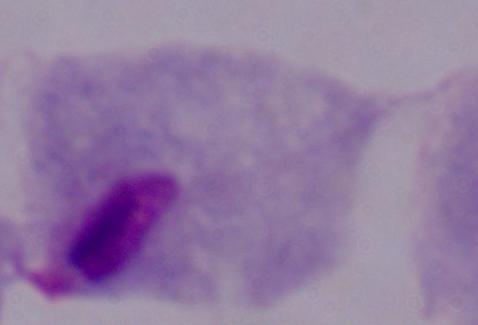

Summary:
  - Identification: trichomonad
  - Magnification: 1000x
  - Modality: micrograph